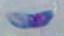

Toxoplasma gondii is seen. Photomicrograph. Captured at 1000x magnification.